Assess the morphology of the erythrocytes.
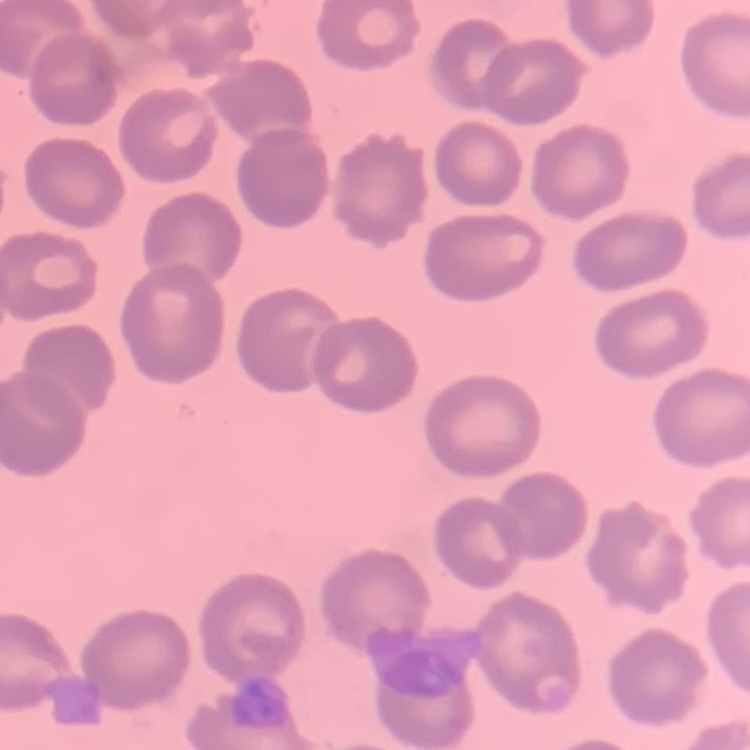
No rouleaux formation.

image_type: square crop of a larger photomicrograph
stain: Field's or Giemsa
preparation: thin blood film